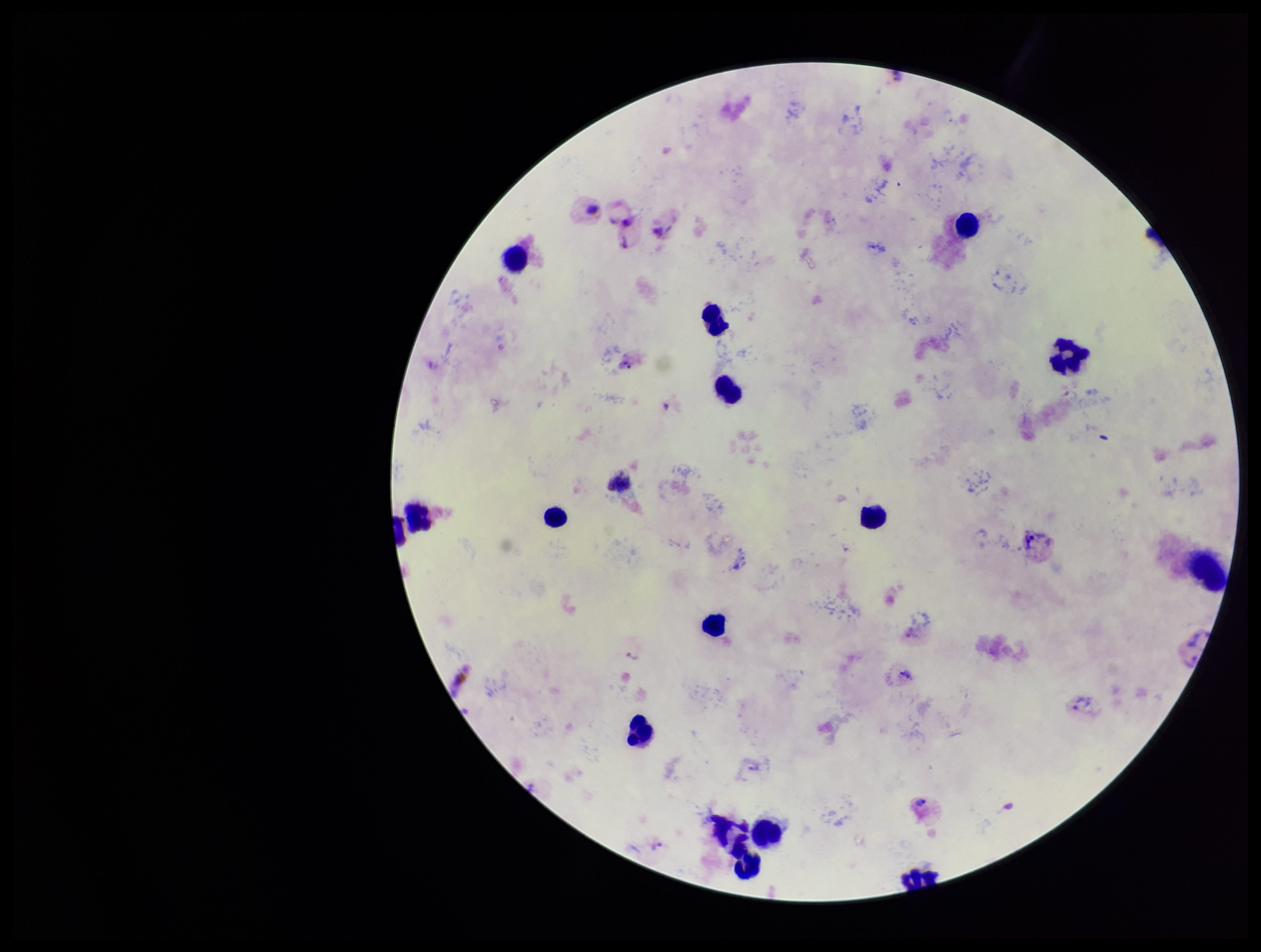 Image is 1261×952 pixels. Parasite count: 10. Leukocyte count: 14. Giemsa stain. Smartphone photograph taken through the eyepiece of a microscope. Species reported for this patient: Plasmodium vivax. Plasmodium parasites: identified. Preparation: thick. Patient malaria status: positive. Single field of view.